Classify this cell by malaria status.
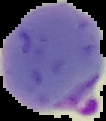

Parasitized.

image size = 106×121 pixels
image type = cell region segmented out of the field of view; surrounding area masked to black
preparation = thin blood smear